Assess this cell for malaria.
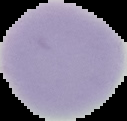
It is uninfected.

Summary:
  - Image size: 127×121 pixels
  - Preparation: thin blood smear
  - Image type: segmented cell region with the area outside set to black